Name the parasite shown.
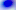

This is Toxoplasma gondii.

Summary:
  - Modality: photomicrograph
  - Magnification: 400x